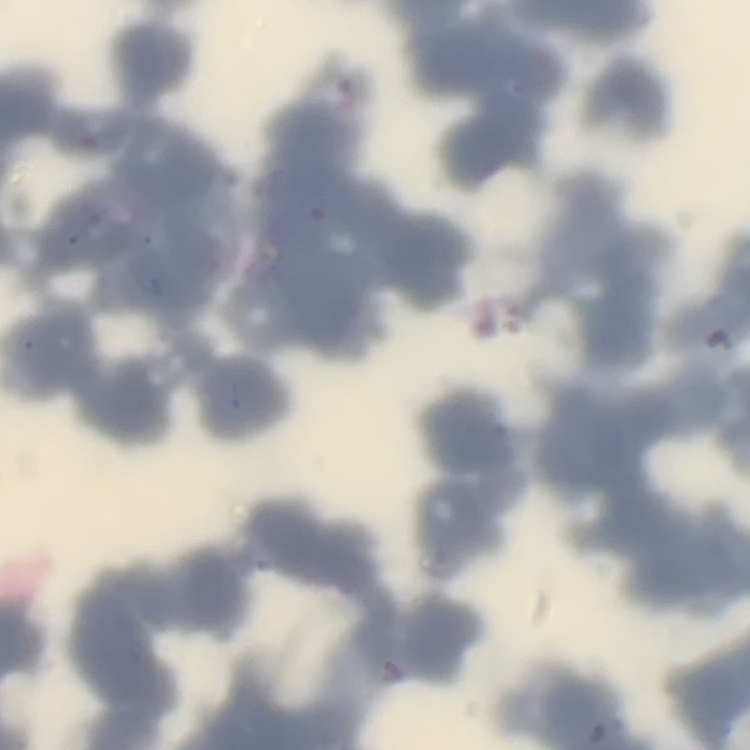 The red blood cells show rouleaux formation. Field's or Giemsa stain. Square crop of a larger photomicrograph. Thin blood smear.